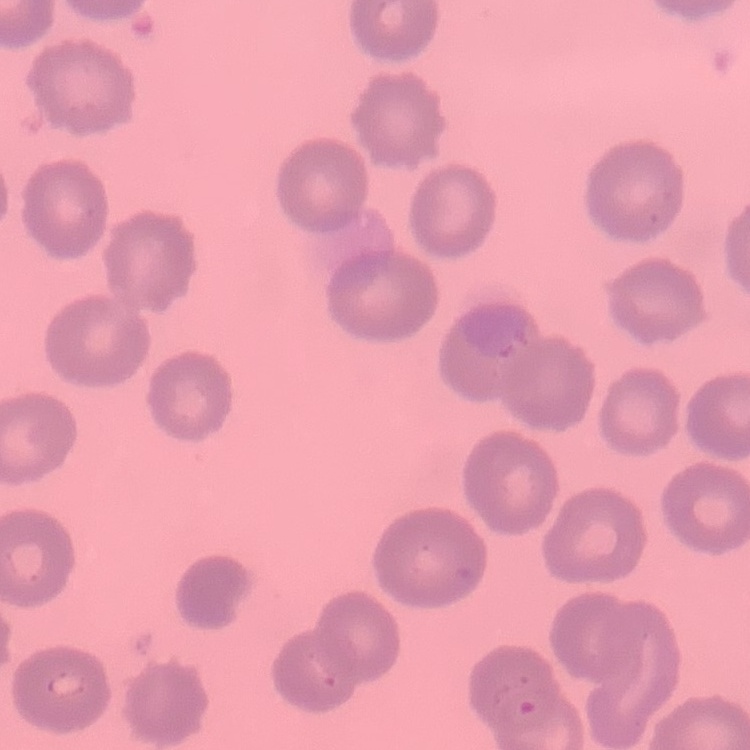
erythrocyte morphology = no rouleaux formation
stain = Field's or Giemsa
preparation = thin peripheral smear
image type = one tile cut from a larger photomicrograph